Comment on the morphology of the erythrocytes.
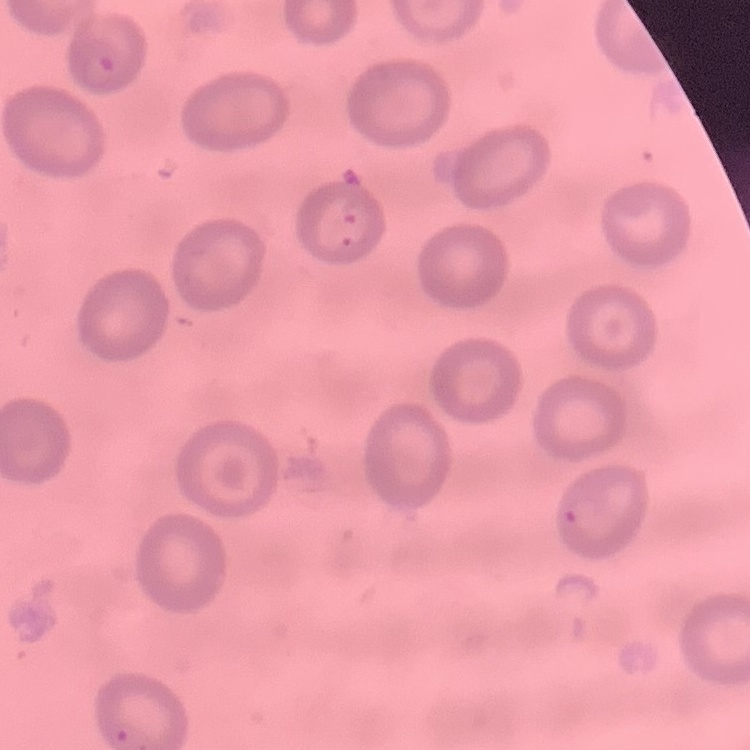

No rouleaux formation.

Field's or Giemsa stain. Square crop of a larger photomicrograph. Thin peripheral smear.